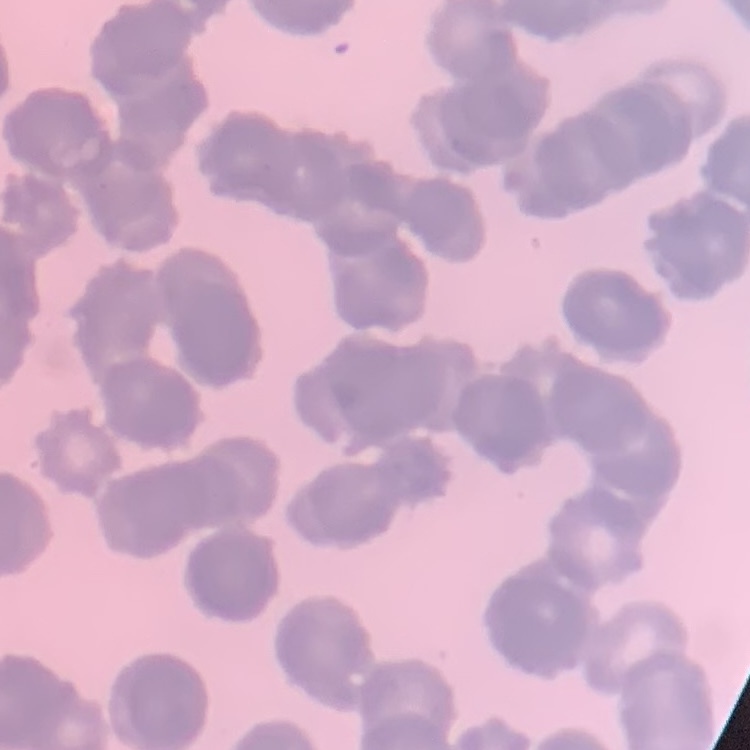

Summary:
  - Red blood cell morphology: rouleaux formation
  - Stain: Field's or Giemsa
  - Preparation: thin peripheral smear
  - Image type: one tile cut from a larger photomicrograph